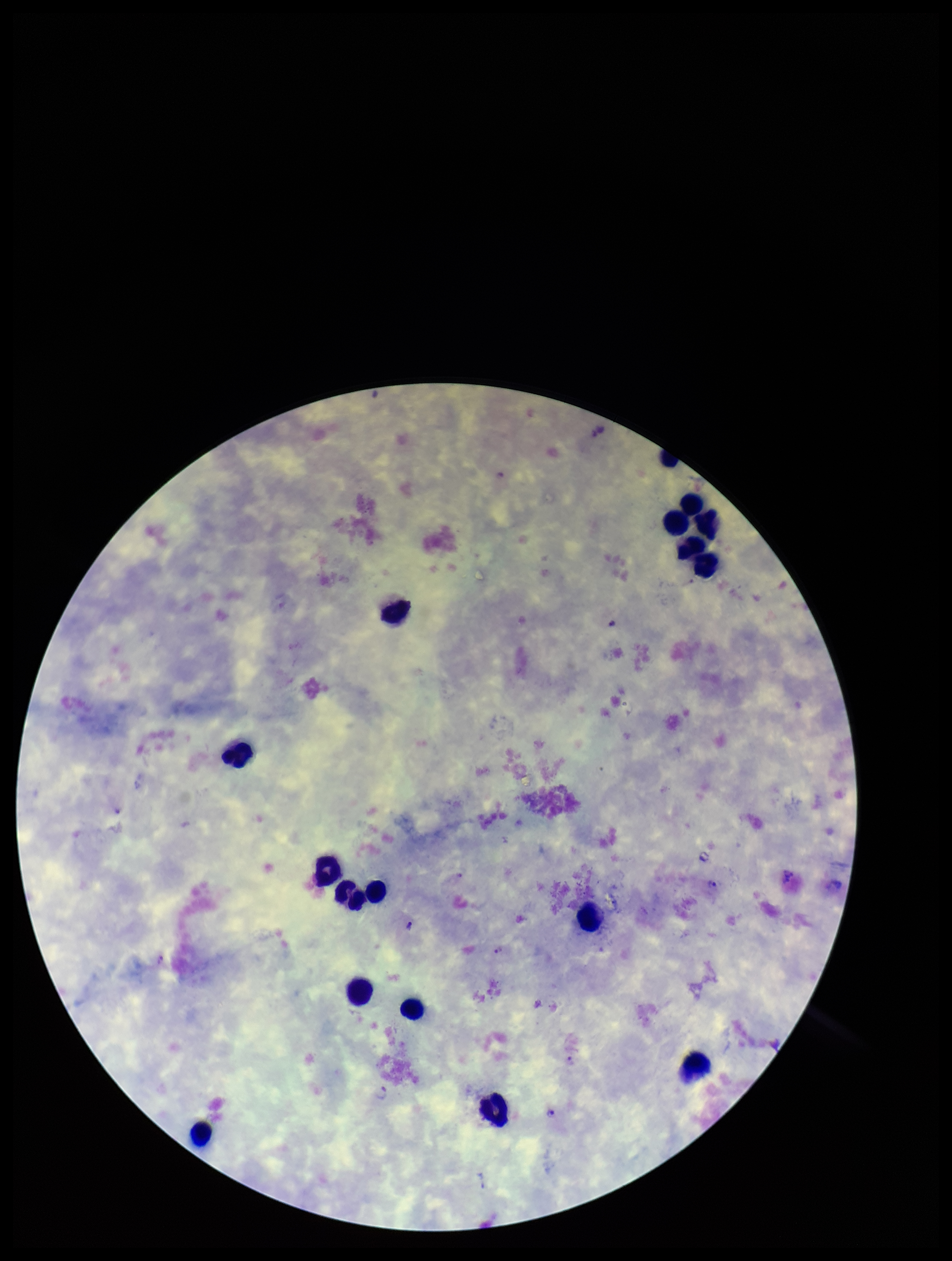
patient malaria status = positive
image size = 952×1261 pixels
preparation = thick blood smear
Plasmodium parasites = identified
capture = smartphone photograph through the microscope eyepiece
parasite count = 7
field of view = single
species reported for this patient = Plasmodium vivax
leukocyte count = 17
stain = Giemsa